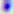
magnification = 400x
modality = photomicrograph
identification = Toxoplasma gondii